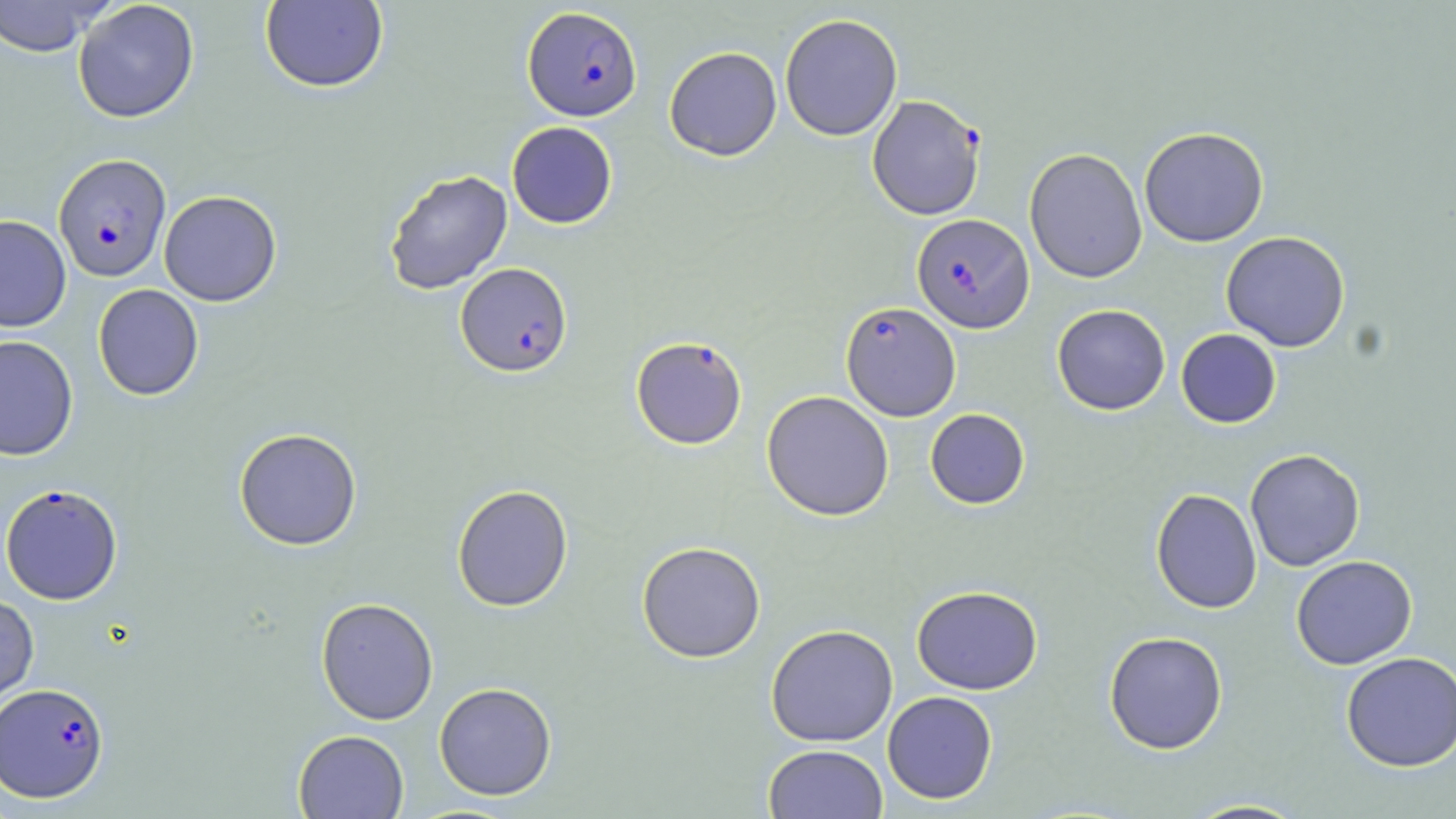
slide_level_diagnosis: Plasmodium falciparum
preparation: thin blood smear
plasmodium_falciparum_infected_red_blood_cell_locations: 'approximate bounding boxes as (x1,y1)-(x2,y2) corner pairs in pixels: (522,7)-(642,120), (866,94)-(986,222), (53,153)-(171,282), (912,213)-(1034,333), (455,262)-(573,377), (841,301)-(961,421), (631,336)-(748,449), (0,483)-(123,604), (1,682)-(109,803)'
magnification: 1000x
image_size: 1456×819 pixels
stain: May-Grünwald-Giemsa
modality: light microscopy
field_of_view: single
uninfected_red_blood_cell_locations: 'approximate bounding boxes as (x1,y1)-(x2,y2) corner pairs in pixels: (73,0)-(200,123), (0,1)-(113,57), (259,1)-(388,93), (779,13)-(903,141), (664,46)-(782,161), (506,121)-(618,229), (1139,126)-(1269,247), (1024,148)-(1147,283), (384,169)-(512,294), (159,190)-(282,306), (0,214)-(72,332), (1221,231)-(1350,352), (93,284)-(204,400), (1052,304)-(1170,415), (1176,328)-(1281,428), (0,334)-(78,461), (761,390)-(894,521), (925,408)-(1030,509), (234,427)-(362,550), (1244,449)-(1365,572), (452,483)-(574,612), (1150,488)-(1262,614), (636,541)-(766,663), (1291,555)-(1418,670), (911,585)-(1043,695), (0,593)-(39,711), (316,597)-(439,725), (765,624)-(898,746), (1104,630)-(1228,755), (1340,652)-(1456,772), (434,682)-(558,800), (882,691)-(998,804), (293,729)-(409,819), (763,744)-(888,819), (1180,798)-(1312,818)'